Give the position of every malaria parasite.
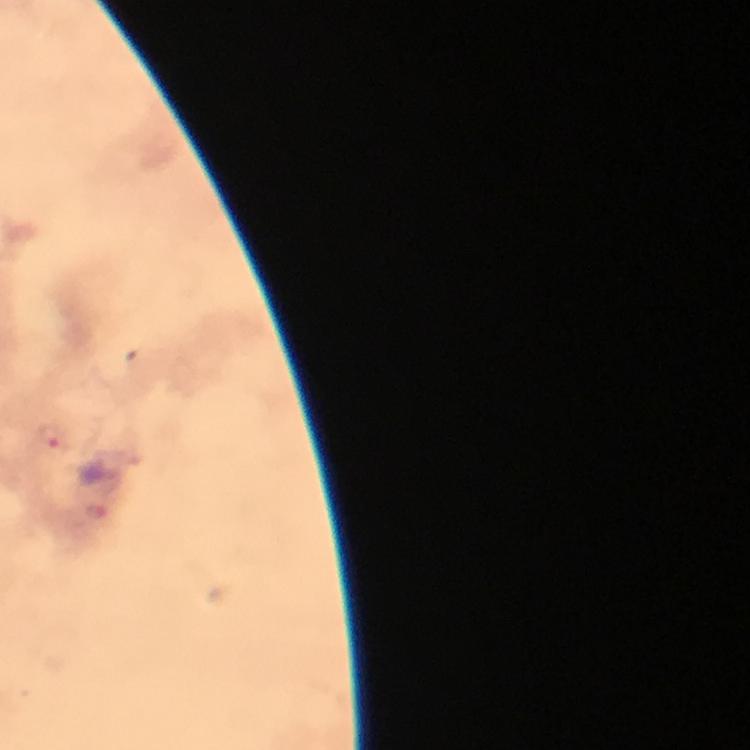
Approximate centers as (x, y) in pixels.
Malaria parasites: (53, 436), (95, 512).

{
  "capture": "smartphone camera through the microscope",
  "context": "from a malaria diagnostic workup",
  "image_size": "750×750 pixels",
  "cropped_from": "one field of view",
  "preparation": "thick smear",
  "immersion_oil": "used",
  "magnification": "100x",
  "stain": "Giemsa"
}